Report the malaria status.
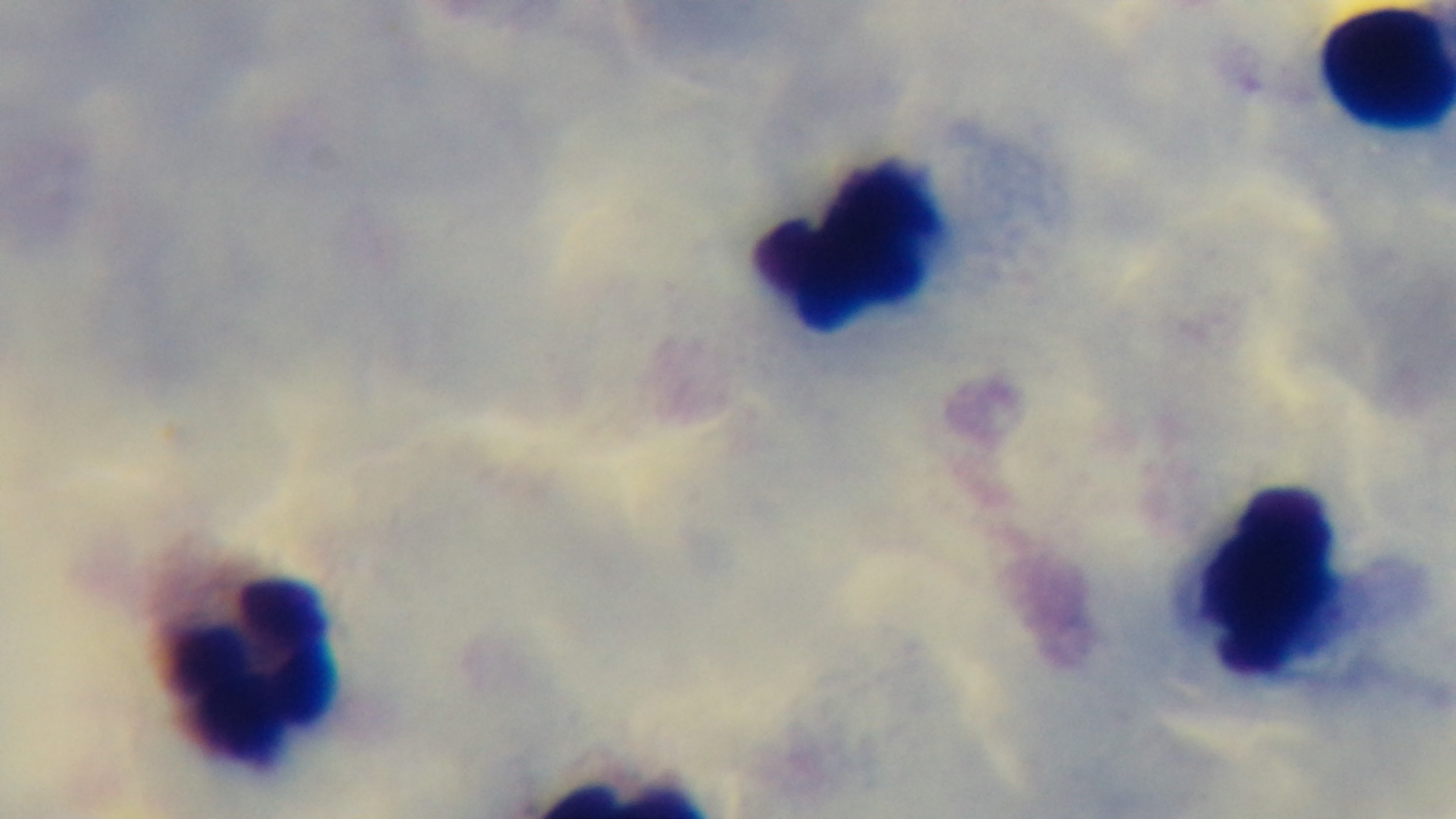
Uninfected.

Single field of view. Giemsa stain. Oil-immersion objective, 100x. Light microscopy. Mounted 4K digital camera. Preparation: thick blood film.